Locate every Plasmodium parasite and every leukocyte.
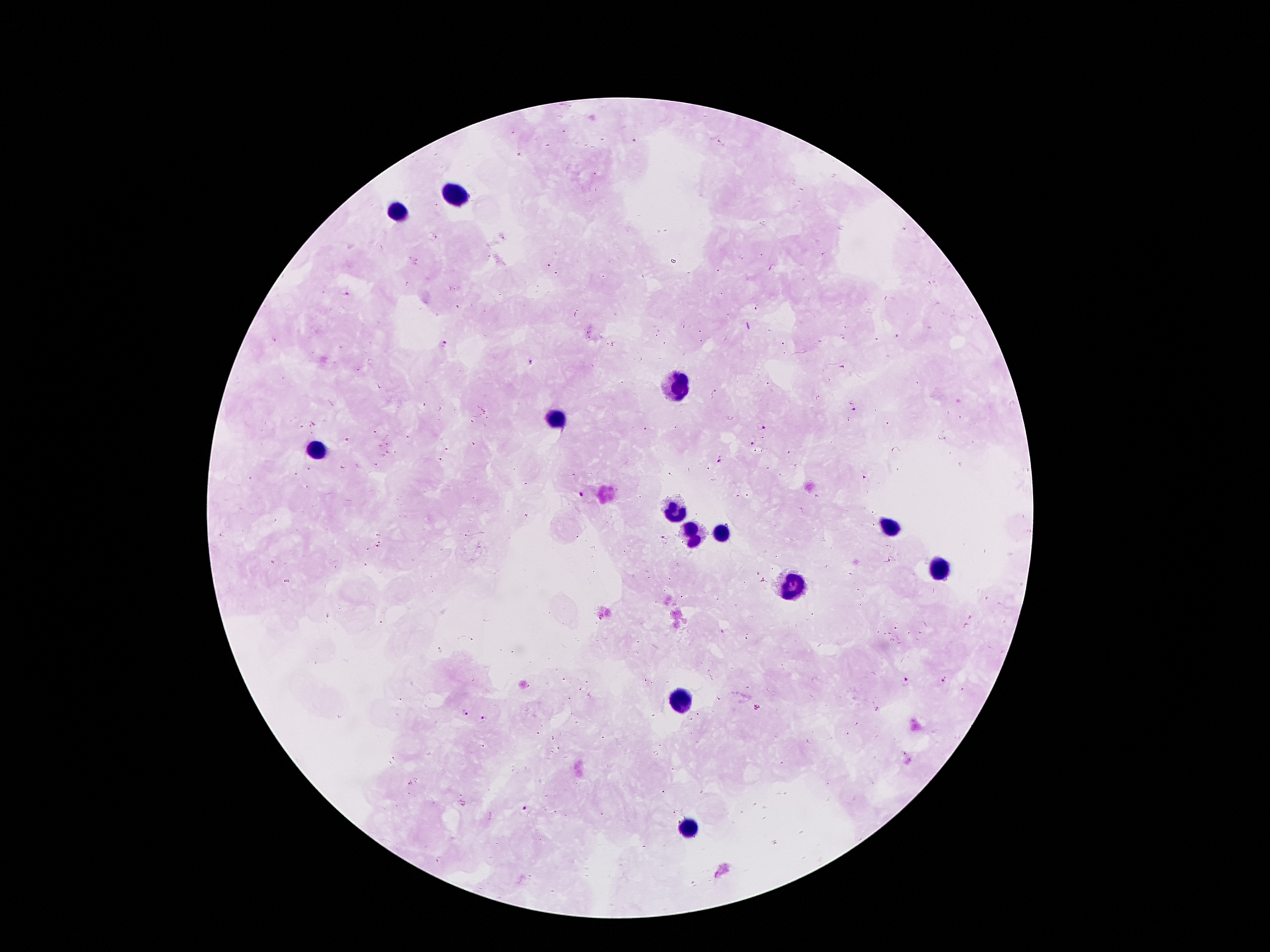

Approximate centers as (x, y) in pixels.
Plasmodium parasites: (633, 140), (520, 155), (549, 266), (773, 267), (557, 274), (346, 295), (757, 308), (577, 314), (700, 332), (587, 333), (897, 335), (842, 336), (591, 339), (275, 341), (784, 344), (445, 345), (532, 362), (843, 368), (717, 391), (818, 398), (853, 409), (848, 419), (761, 426), (645, 429), (376, 432), (408, 438), (347, 439), (752, 441), (388, 444), (446, 449), (788, 453), (388, 454), (441, 460), (721, 461), (377, 464), (343, 468), (669, 474), (864, 478), (581, 496), (818, 496), (527, 516), (467, 536), (664, 539), (379, 544), (888, 560), (763, 582), (896, 628), (723, 632), (945, 681), (906, 682), (717, 698), (756, 707), (878, 709), (466, 713), (486, 719), (410, 783), (525, 808).
Leukocytes: (453, 192), (393, 214), (678, 388), (557, 418), (317, 452), (678, 508), (890, 528), (722, 532), (694, 534), (938, 570), (788, 586), (679, 702), (688, 828).

Summary:
  - Image size: 1270×952 pixels
  - Capture: smartphone through the microscope eyepiece
  - Magnification: 100x
  - Preparation: thick blood film
  - Field of view: one from this slide
  - Patient malaria status: infected with Plasmodium falciparum
  - Stain: Giemsa